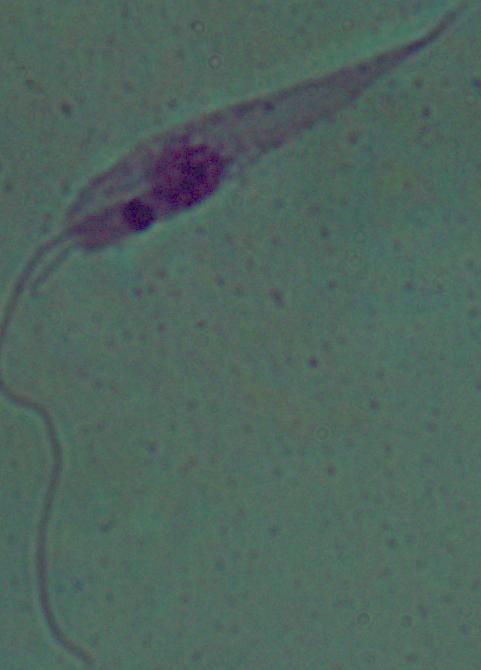

Summary:
  - Magnification: 1000x
  - Modality: micrograph
  - Identification: Leishmania